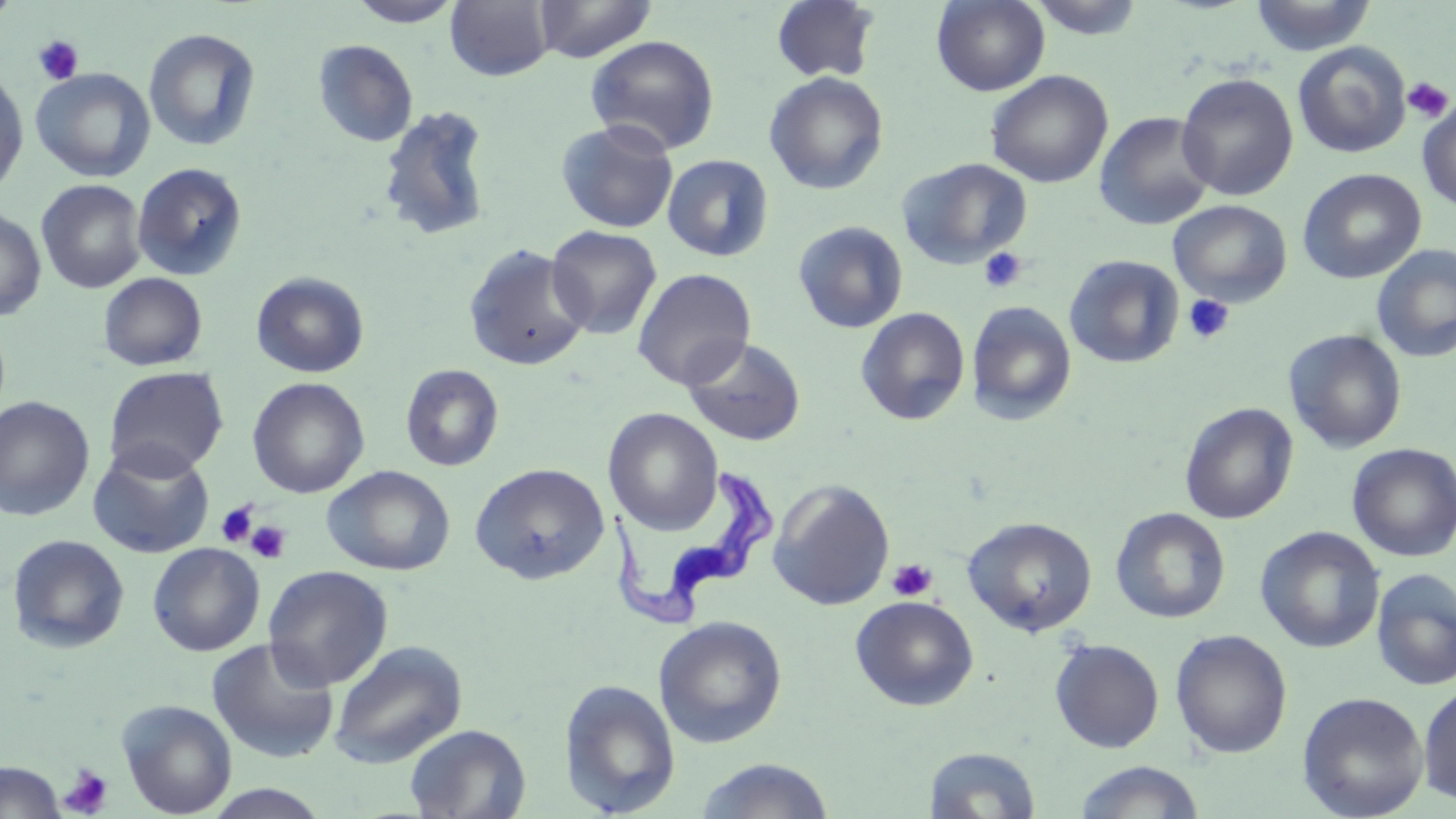
Summary:
  - Coordinate format: approximate bounding boxes as (x1, y1, x2, y2) in pixels
  - Platelet locations: (33, 35, 84, 86), (1402, 76, 1454, 123), (978, 247, 1027, 294), (1183, 294, 1235, 344), (217, 500, 258, 548), (246, 520, 290, 563), (886, 558, 938, 602), (58, 765, 113, 817)
  - Uninfected red blood cell locations: (0, 0, 21, 29), (533, 0, 657, 62), (770, 0, 880, 83), (931, 0, 1050, 96), (1027, 0, 1147, 40), (1249, 0, 1377, 56), (346, 1, 463, 28), (445, 1, 553, 81), (143, 27, 262, 152), (585, 35, 720, 155), (312, 39, 418, 148), (1293, 41, 1411, 158), (0, 66, 29, 197), (30, 68, 155, 183), (985, 70, 1113, 188), (764, 72, 888, 195), (1176, 73, 1298, 200), (1417, 100, 1456, 213), (377, 105, 495, 242), (1094, 111, 1216, 231), (555, 118, 679, 234), (662, 154, 774, 261), (897, 157, 1033, 269), (131, 162, 248, 282), (1298, 168, 1427, 284), (36, 179, 147, 294), (1168, 200, 1292, 306), (0, 207, 47, 322), (792, 221, 908, 334), (546, 225, 662, 339), (462, 244, 591, 371), (1371, 245, 1456, 362), (1064, 255, 1184, 369), (631, 268, 756, 390), (250, 271, 369, 378), (98, 272, 208, 372), (967, 301, 1077, 425), (856, 307, 970, 426), (1283, 328, 1407, 453), (682, 336, 807, 446), (400, 364, 504, 472), (103, 366, 228, 479), (247, 377, 369, 498), (0, 396, 96, 521), (1180, 401, 1298, 524), (604, 408, 723, 535), (87, 441, 215, 559), (1347, 443, 1456, 562), (471, 463, 609, 584), (322, 465, 455, 576), (768, 480, 895, 610), (1110, 508, 1230, 624), (962, 516, 1098, 636), (1255, 526, 1384, 653), (6, 534, 130, 654), (147, 542, 265, 656), (262, 565, 393, 691), (1371, 568, 1456, 691), (850, 595, 978, 711), (653, 615, 787, 748), (1170, 629, 1293, 759), (207, 638, 340, 764), (1049, 638, 1164, 753), (328, 640, 468, 769), (559, 678, 682, 816), (1417, 682, 1456, 807), (1297, 691, 1429, 818), (116, 699, 238, 818), (404, 723, 531, 819), (923, 746, 1042, 818), (695, 758, 835, 818), (1075, 760, 1205, 819), (0, 761, 65, 819), (204, 785, 332, 819)
  - Trypanosoma brucei locations: (598, 464, 777, 635)
  - Slide-level diagnosis: Trypanosoma brucei
  - Field of view: one of a larger specimen
  - Modality: light microscopy
  - Magnification: 1000x
  - Preparation: thin blood smear
  - Image size: 1456×819 pixels
  - Stain: May-Grünwald-Giemsa